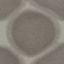
Summary:
  - Result: negative for malaria parasites
  - Capture: smartphone through the microscope eyepiece
  - Stain: Giemsa
  - Image type: cell patch, automatically extracted from a larger field of view and resized to 64 × 64 pixels
  - Preparation: thin smear